Name the parasite shown.
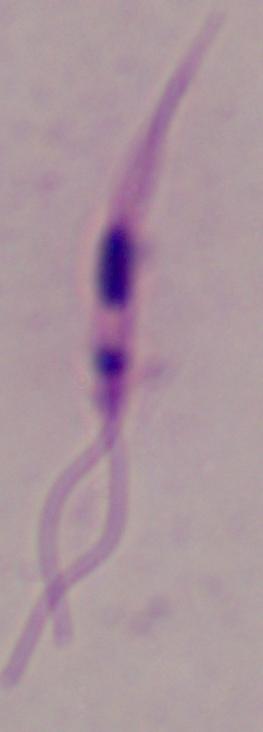

This is Leishmania.

1000x magnification. Micrograph.